Classify this cell by malaria status.
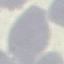
It is uninfected.

Acquired by smartphone through the microscope eyepiece. Thin blood film. Giemsa-stained preparation. Cell patch, automatically extracted from a larger field of view and resized to 64 × 64 pixels.